Outline each blood parasite and name the species.
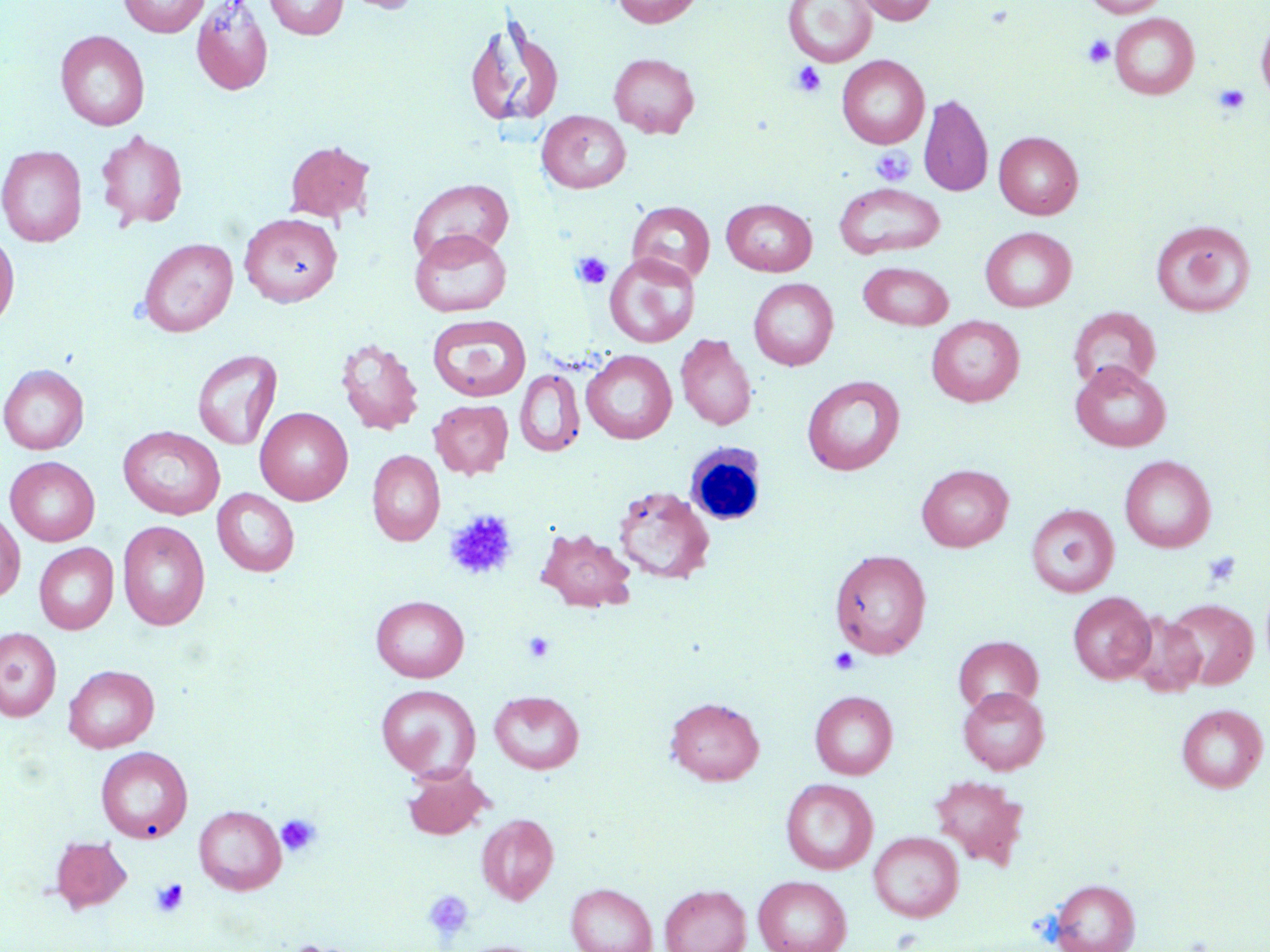

No blood parasites seen.

slide_level_diagnosis: negative for blood parasites
uninfected_red_blood_cell_locations: 'approximate bounding boxes as (x1, y1, x2, y2) in pixels: (119, 0, 210, 37), (190, 0, 274, 96), (264, 0, 348, 39), (340, 0, 422, 14), (612, 0, 702, 28), (783, 0, 877, 67), (851, 0, 939, 25), (1083, 0, 1169, 17), (1109, 13, 1200, 99), (1256, 15, 1270, 107), (464, 18, 565, 131), (55, 30, 150, 131), (609, 53, 700, 138), (837, 55, 929, 148), (919, 94, 993, 197), (537, 111, 632, 194), (95, 129, 188, 231), (994, 131, 1083, 219), (284, 141, 374, 223), (0, 145, 87, 246), (408, 178, 514, 264), (833, 183, 945, 259), (721, 199, 817, 276), (627, 201, 715, 285), (239, 212, 342, 308), (1151, 220, 1256, 317), (980, 227, 1076, 312), (409, 228, 512, 317), (0, 230, 19, 330), (138, 238, 238, 336), (604, 253, 700, 347), (858, 261, 954, 330), (749, 278, 838, 370), (1068, 306, 1161, 392), (427, 314, 530, 401), (927, 316, 1024, 406), (676, 334, 757, 430), (335, 337, 424, 436), (192, 349, 283, 451), (581, 350, 677, 444), (1071, 362, 1170, 452), (0, 364, 89, 454), (515, 368, 585, 457), (802, 375, 905, 476), (429, 400, 514, 479), (255, 407, 353, 505), (118, 426, 225, 520), (367, 450, 444, 546), (1119, 455, 1216, 552), (5, 456, 100, 546), (916, 464, 1013, 551), (612, 485, 715, 585), (213, 489, 299, 576), (1026, 504, 1119, 597), (0, 509, 25, 603), (117, 520, 210, 630), (537, 527, 637, 613), (34, 544, 119, 634), (829, 549, 932, 658), (1068, 592, 1156, 683), (370, 595, 469, 683), (1164, 598, 1258, 690), (1125, 612, 1207, 698), (0, 627, 61, 722), (953, 635, 1043, 714), (64, 664, 159, 752), (376, 685, 480, 780), (958, 687, 1050, 774), (810, 690, 898, 779), (489, 691, 584, 774), (665, 696, 765, 785), (1177, 704, 1268, 792), (95, 746, 193, 842), (402, 765, 493, 840), (929, 775, 1029, 869), (781, 778, 878, 875), (194, 805, 286, 895), (477, 814, 559, 905), (869, 831, 964, 922), (51, 836, 133, 913), (753, 875, 852, 952), (1050, 879, 1140, 952), (566, 883, 657, 952), (659, 884, 751, 952), (273, 939, 371, 952)'
white_blood_cell_locations: 'approximate bounding boxes as (x1, y1, x2, y2) in pixels: (686, 444, 770, 530)'
modality: optical microscopy
magnification: 1000x
field_of_view: one of a larger specimen
image_size: 1270×952 pixels
preparation: thin blood film
stain: May-Grünwald-Giemsa
platelet_locations: 'approximate bounding boxes as (x1, y1, x2, y2) in pixels: (1082, 34, 1115, 68), (790, 62, 827, 97), (1213, 85, 1250, 115), (870, 147, 915, 186), (571, 251, 612, 290), (444, 510, 517, 581), (1202, 551, 1242, 588), (522, 631, 556, 663), (829, 648, 860, 674), (277, 813, 322, 857), (151, 878, 189, 917), (422, 889, 474, 942)'